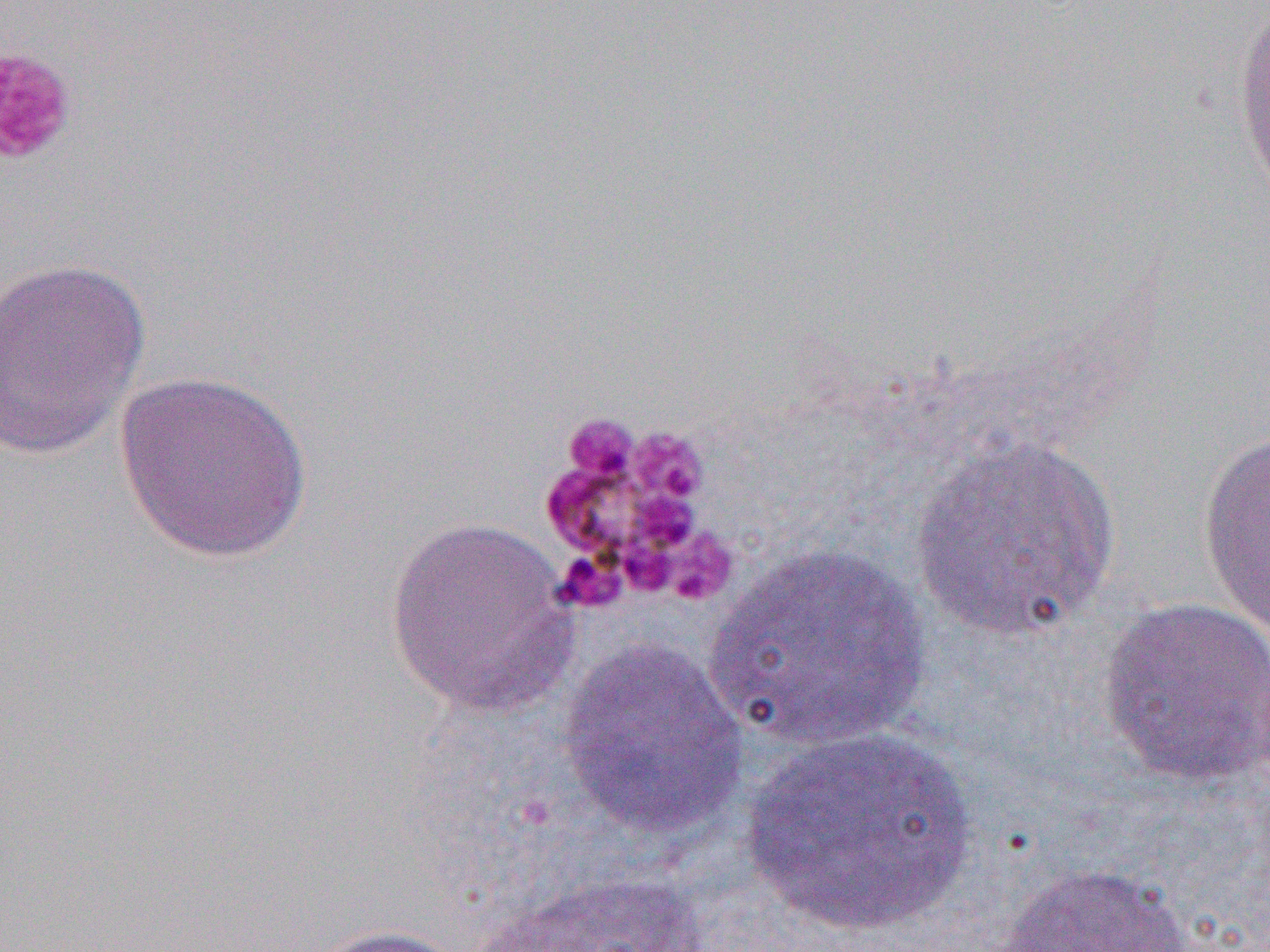
slide_level_diagnosis: Plasmodium malariae
modality: light microscopy
field_of_view: one of a larger specimen
image_size: 1270×952 pixels
platelet_locations: 'approximate bounding boxes as named x1/y1/x2/y2 corners in pixels: (x1=0, y1=45, x2=78, y2=168), (x1=560, y1=412, x2=641, y2=490), (x1=555, y1=550, x2=627, y2=613)'
uninfected_red_blood_cell_locations: 'approximate bounding boxes as named x1/y1/x2/y2 corners in pixels: (x1=1230, y1=0, x2=1270, y2=205), (x1=0, y1=257, x2=151, y2=460), (x1=114, y1=369, x2=314, y2=564), (x1=1198, y1=431, x2=1270, y2=635), (x1=912, y1=436, x2=1122, y2=640), (x1=383, y1=514, x2=579, y2=717), (x1=703, y1=543, x2=934, y2=751), (x1=1097, y1=596, x2=1270, y2=787), (x1=558, y1=638, x2=750, y2=841), (x1=744, y1=725, x2=977, y2=935), (x1=993, y1=861, x2=1197, y2=952), (x1=468, y1=870, x2=717, y2=952), (x1=296, y1=923, x2=473, y2=952)'
preparation: thin blood smear
magnification: 1000x